Comment on the morphology of the red blood cells.
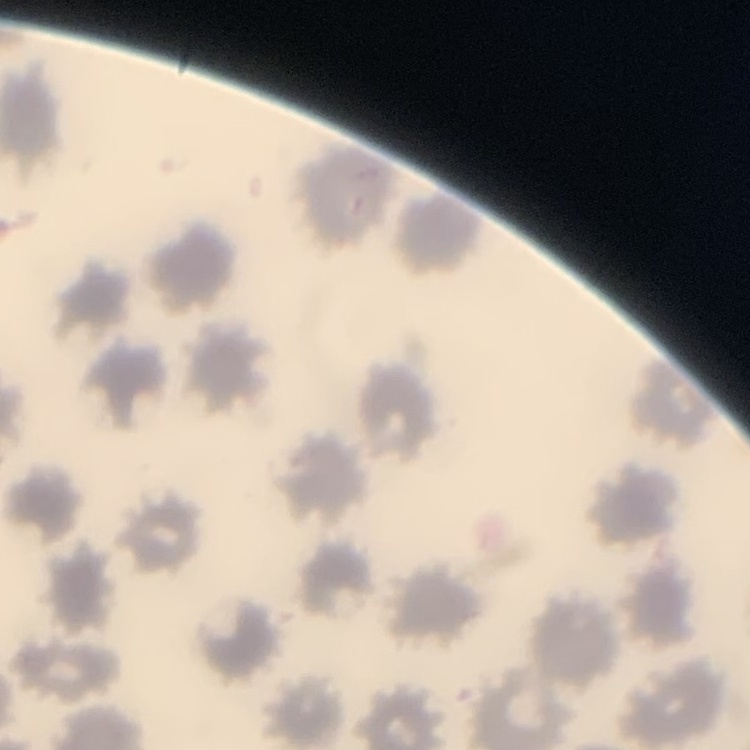
They show no rouleaux formation.

{
  "stain": "Field's or Giemsa",
  "preparation": "thin peripheral smear",
  "image_type": "one tile cut from a larger photomicrograph"
}